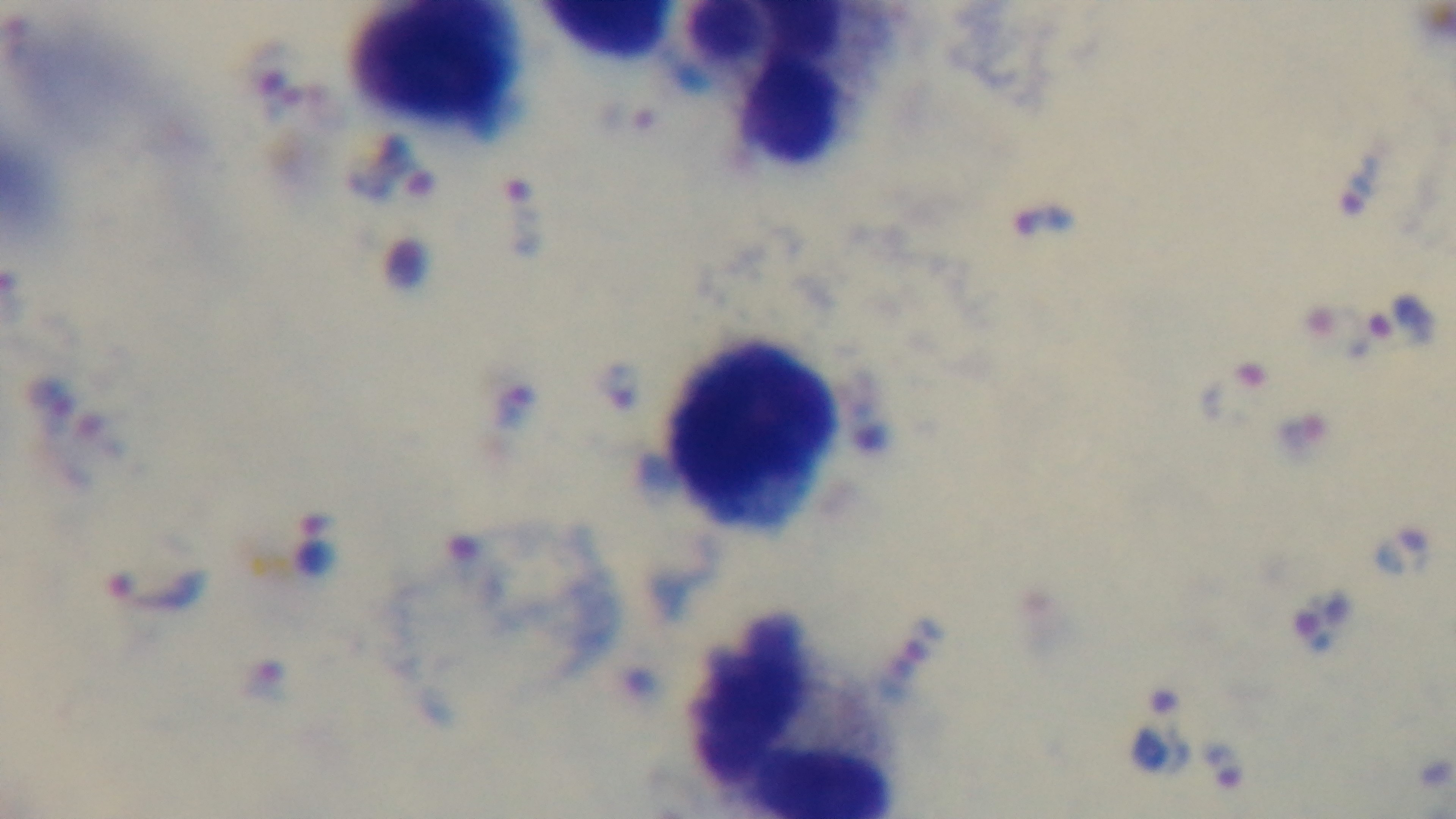

Preparation: thick. One field from the slide. Malaria status: infected. Photomicrograph. Mounted 4K digital camera. 100x oil-immersion objective. Giemsa-stained.